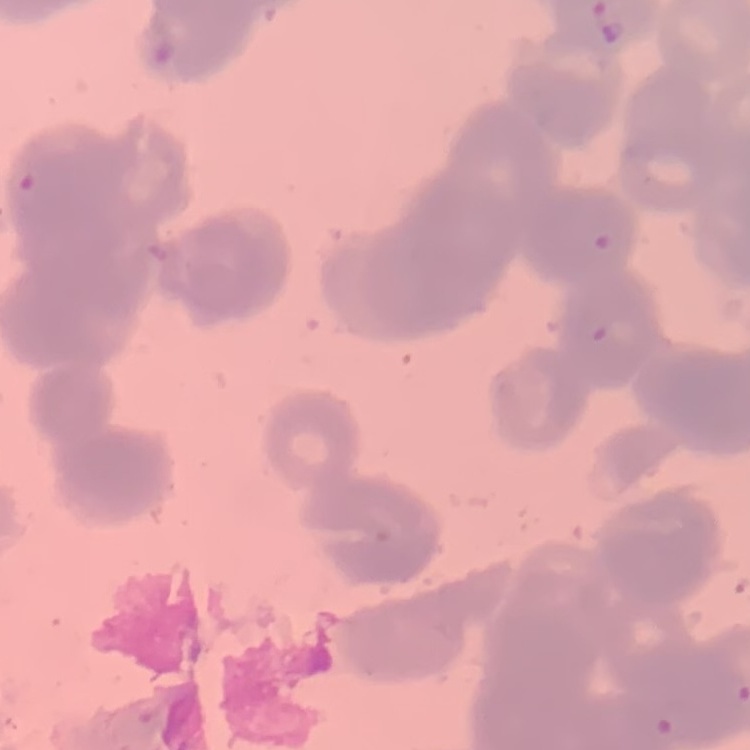

red blood cell morphology = rouleaux formation
image type = one tile cut from a larger photomicrograph
stain = Field's or Giemsa
preparation = thin blood film